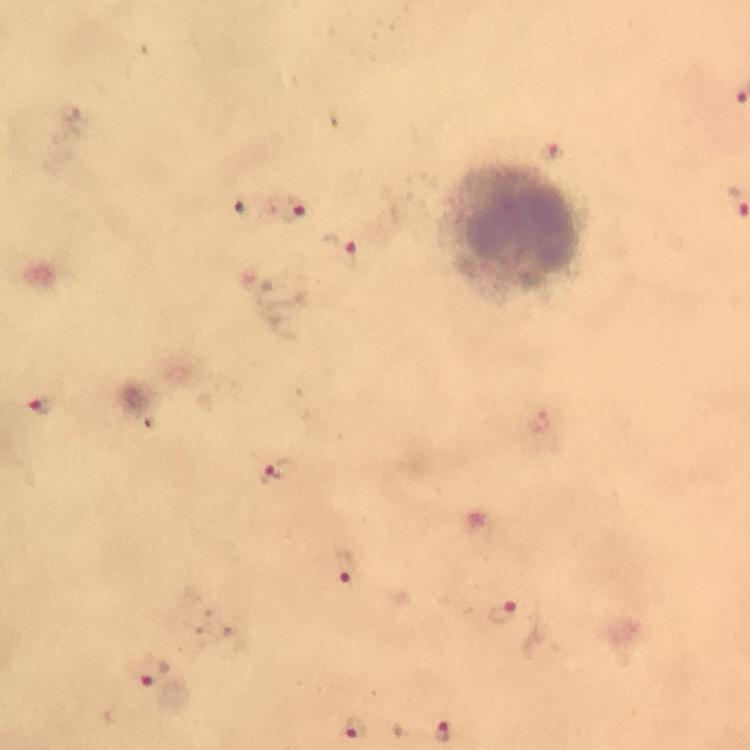
{
  "capture": "smartphone camera through the microscope",
  "plasmodium_parasite_locations": "approximate centers as {x, y} in pixels: {552, 151}, {290, 212}, {342, 252}, {269, 296}, {39, 407}, {275, 472}, {346, 567}, {502, 612}, {145, 676}, {355, 728}, {441, 730}",
  "context": "from a diagnostic examination for malaria",
  "magnification": "100x",
  "cropped_from": "a single field of view",
  "immersion_oil": "used",
  "preparation": "thick blood film",
  "image_size": "750×750 pixels",
  "leukocyte_locations": "approximate centers as {x, y} in pixels: {512, 230}",
  "stain": "Giemsa"
}